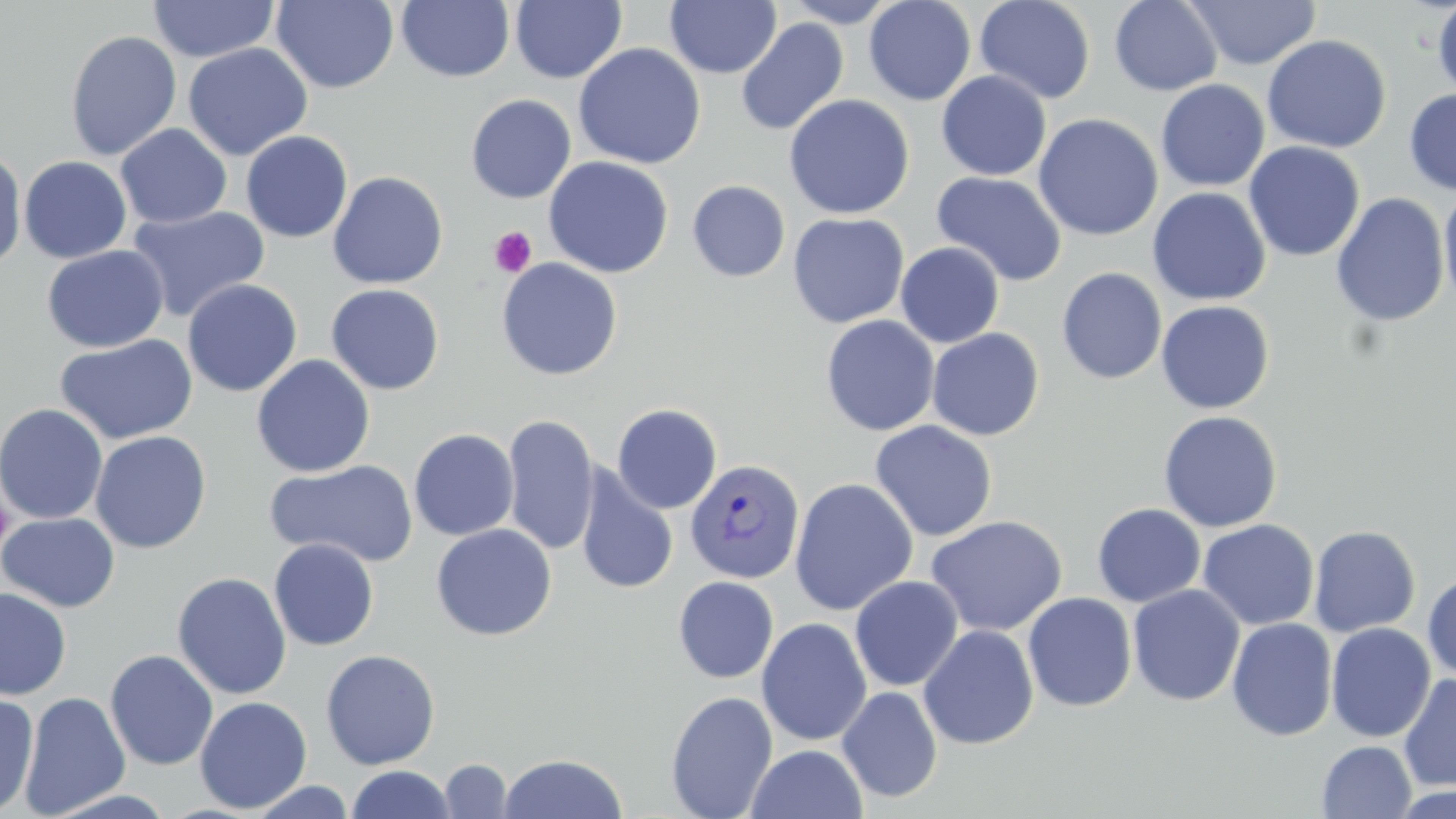 Approximate bounding boxes as (x1,y1)-(x2,y2) corner pairs in pixels. Uninfected red blood cell locations: (271,0)-(399,93), (397,0)-(514,82), (781,0)-(901,27), (864,0)-(976,105), (975,0)-(1095,104), (1185,0)-(1321,70), (1432,0)-(1456,102), (147,1)-(279,62), (510,1)-(627,84), (666,1)-(781,78), (1109,1)-(1223,96), (735,18)-(849,136), (65,30)-(182,161), (1261,34)-(1392,154), (183,42)-(313,160), (573,43)-(706,169), (936,71)-(1052,181), (1156,79)-(1270,192), (1403,88)-(1456,196), (466,94)-(576,204), (784,94)-(914,219), (1033,113)-(1163,241), (116,123)-(232,229), (240,130)-(353,243), (1244,141)-(1365,262), (0,148)-(27,272), (19,155)-(132,264), (543,156)-(674,278), (328,171)-(448,289), (932,171)-(1067,286), (687,180)-(791,282), (1438,184)-(1456,315), (1147,187)-(1272,306), (1331,192)-(1450,327), (127,205)-(270,323), (788,212)-(909,328), (895,242)-(1004,348), (42,245)-(169,353), (496,258)-(623,380), (1057,267)-(1167,384), (182,278)-(302,397), (326,283)-(445,395), (1155,300)-(1275,414), (821,315)-(940,436), (927,328)-(1045,441), (54,334)-(198,445), (251,354)-(375,478), (0,404)-(108,524), (613,404)-(722,514), (1158,410)-(1283,533), (503,414)-(599,556), (870,420)-(997,542), (409,428)-(519,541), (90,431)-(212,553), (264,459)-(419,568), (575,466)-(679,595), (789,477)-(919,616), (1092,503)-(1206,607), (0,512)-(120,612), (926,515)-(1067,635), (1198,519)-(1319,631), (431,524)-(556,641), (1308,525)-(1421,637), (268,538)-(380,651), (172,571)-(292,700), (1422,572)-(1456,682), (673,576)-(779,684), (849,576)-(963,692), (1128,584)-(1245,706), (0,587)-(72,700), (1022,592)-(1137,712), (756,617)-(872,746), (1226,617)-(1338,742), (1326,622)-(1435,742), (919,624)-(1039,750), (104,649)-(218,771), (320,649)-(440,770), (1398,673)-(1456,792), (837,686)-(942,803), (0,691)-(39,817), (19,691)-(131,817), (666,691)-(778,819), (194,696)-(312,813), (1317,741)-(1417,818), (746,744)-(868,819), (498,753)-(628,818), (439,759)-(513,818), (345,765)-(456,818), (246,780)-(357,818). Platelet locations: (490,225)-(538,277), (1,496)-(15,552). Plasmodium vivax-infected red blood cell locations: (685,459)-(806,584). Slide-level diagnosis: Plasmodium vivax. Captured at 1000x magnification. Light microscopy. Image is 1456×819 pixels. May-Grünwald-Giemsa stain. Thin blood film. One field of a larger specimen.